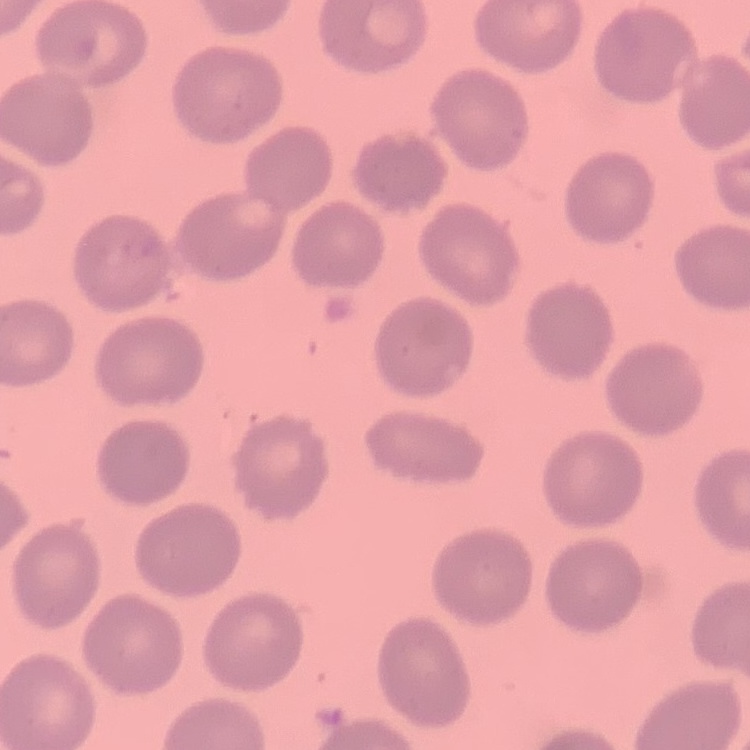 The erythrocytes exhibit no rouleaux formation. Thin peripheral smear. One tile cut from a larger photomicrograph. Stained with either Field's or Giemsa.